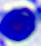

Summary:
  - Modality: photomicrograph
  - Identification: white blood cell
  - Magnification: 400x